Locate every Babesia divergens-infected red blood cell.
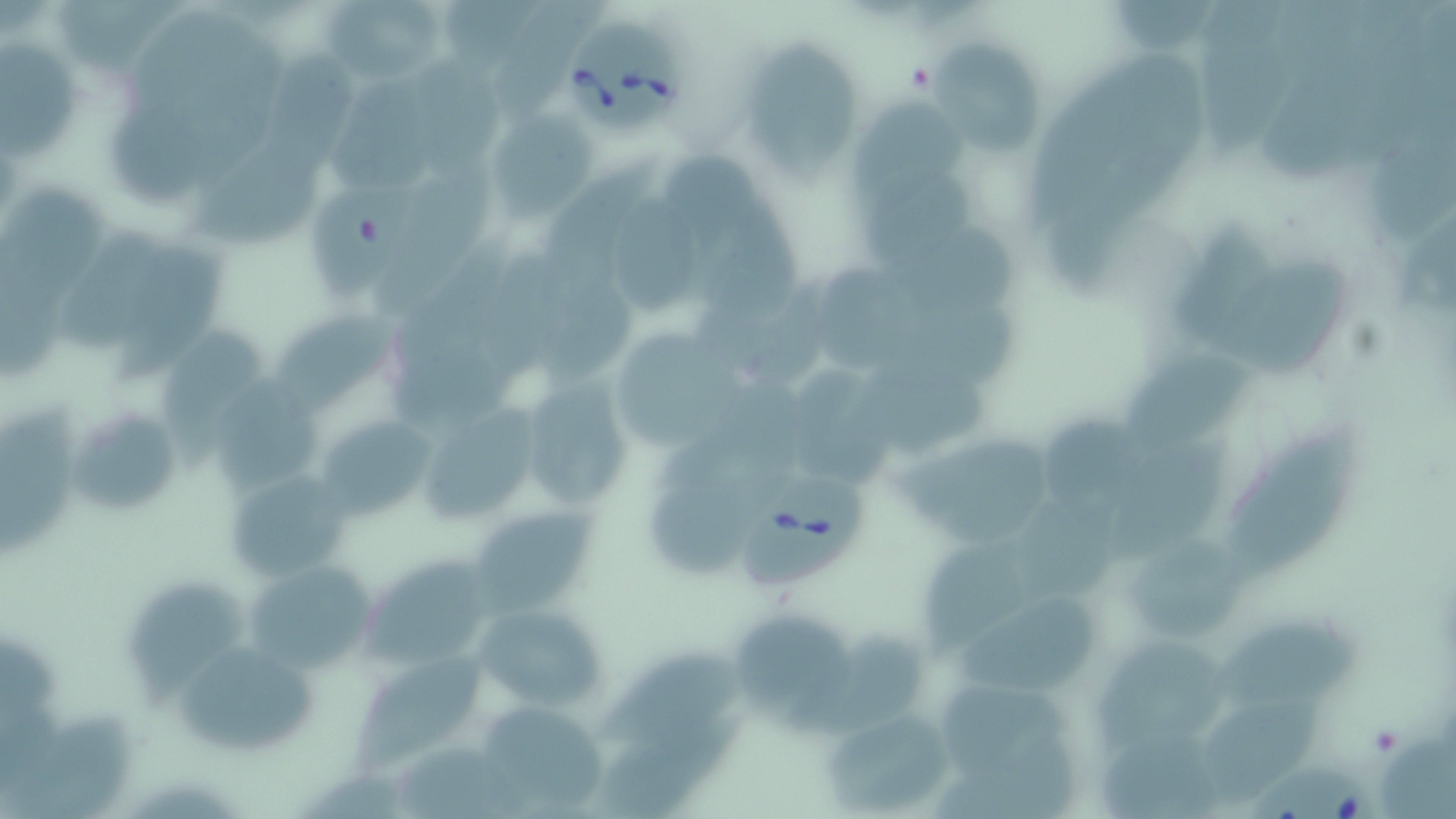
Approximate bounding boxes as (x1, y1, x2, y2) in pixels.
Babesia divergens-infected red blood cells: (562, 17, 687, 139), (733, 473, 866, 598), (1244, 758, 1382, 819).

Uninfected red blood cell locations: (57, 0, 185, 70), (325, 0, 448, 87), (1200, 1, 1303, 159), (0, 47, 84, 164), (930, 47, 1039, 158), (751, 48, 860, 186), (268, 50, 355, 172), (415, 59, 504, 176), (333, 88, 441, 195), (848, 100, 969, 228), (486, 110, 592, 218), (658, 153, 758, 251), (539, 156, 663, 326), (183, 158, 325, 245), (366, 170, 497, 319), (870, 175, 973, 273), (311, 187, 414, 301), (0, 193, 110, 310), (611, 202, 705, 315), (699, 202, 805, 324), (49, 229, 182, 359), (122, 253, 221, 383), (1220, 261, 1352, 376), (813, 274, 921, 377), (893, 306, 1025, 395), (275, 315, 408, 423), (161, 328, 260, 471), (618, 340, 747, 449), (1115, 357, 1251, 452), (851, 364, 992, 457), (791, 371, 897, 487), (518, 377, 635, 516), (0, 398, 75, 558), (68, 402, 185, 519), (412, 403, 544, 525), (314, 413, 440, 520), (1043, 419, 1136, 542), (1227, 431, 1359, 584), (1101, 440, 1234, 571), (895, 444, 1054, 549), (223, 469, 349, 582), (470, 505, 599, 620), (931, 534, 1024, 660), (1130, 541, 1241, 636), (360, 555, 492, 669), (243, 560, 378, 675), (124, 584, 248, 710), (955, 595, 1098, 698), (472, 603, 604, 714), (736, 617, 853, 727), (1219, 624, 1365, 714), (789, 630, 928, 734), (1096, 641, 1229, 755), (175, 649, 323, 755), (595, 651, 747, 751), (352, 655, 488, 777), (942, 686, 1082, 779), (470, 700, 609, 816), (821, 708, 957, 811), (597, 712, 751, 816), (937, 727, 1080, 819), (1379, 730, 1456, 819), (1103, 742, 1222, 819), (400, 744, 531, 818). Slide-level diagnosis: Babesia divergens. Light microscopy. 1000x magnification. May-Grünwald-Giemsa stain. Image is 1456×819 pixels. One field of a larger specimen. Thin blood film.